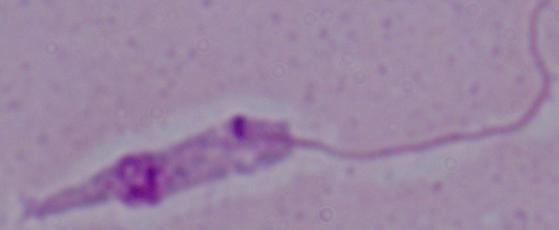 1000x magnification. Photomicrograph. A Leishmania parasite is seen.